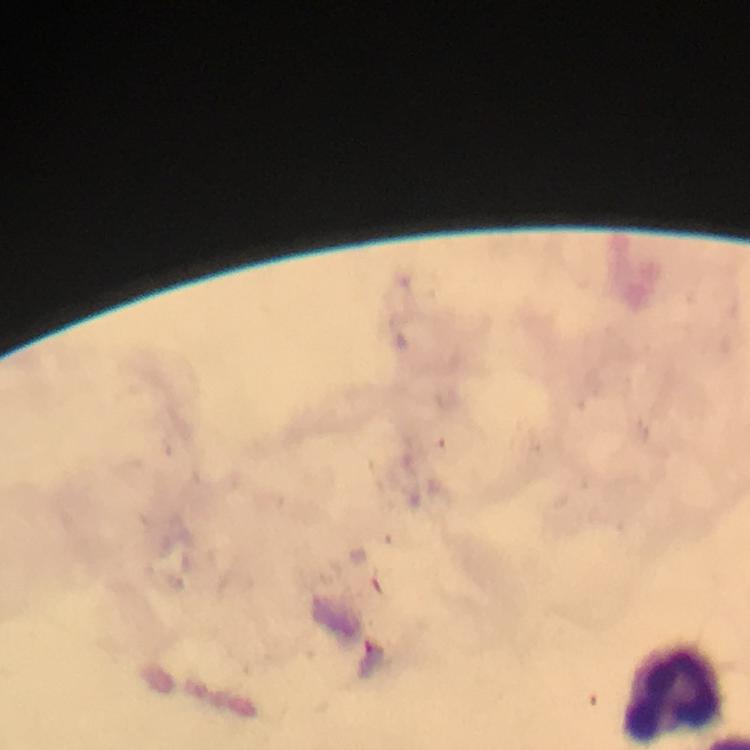

Approximate centers as [x, y] in pixels.
Summary:
  - Leukocyte locations: [673, 691]
  - Preparation: thick smear
  - Immersion oil: used
  - Stain: Giemsa
  - Image size: 750×750 pixels
  - Context: from a diagnostic examination for malaria
  - Magnification: 100x
  - Cropped from: a single field of view
  - Capture: smartphone photograph through a microscope
  - Malaria parasites: none seen